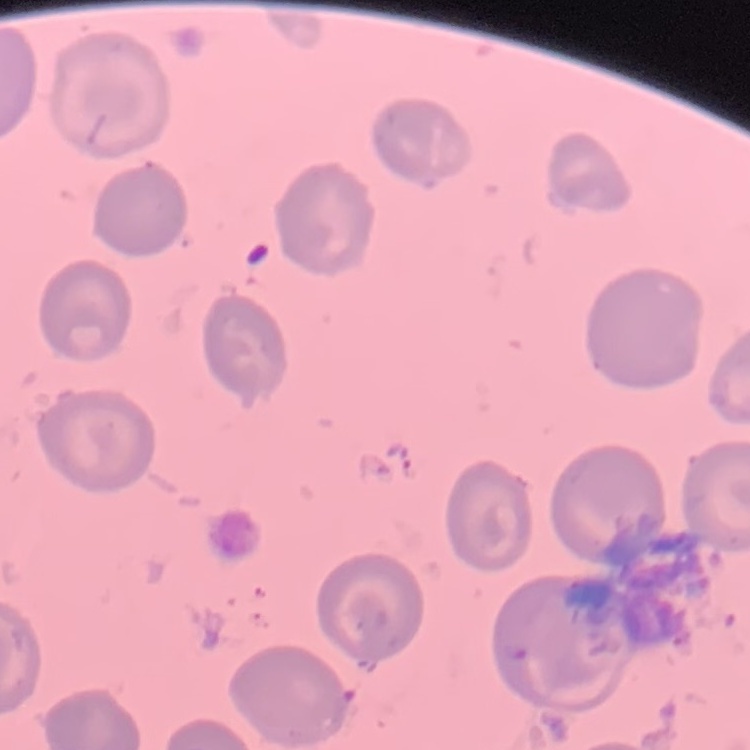

{
  "erythrocyte_morphology": "no rouleaux formation",
  "image_type": "one tile cut from a larger photomicrograph",
  "preparation": "thin peripheral smear",
  "stain": "Field's or Giemsa"
}